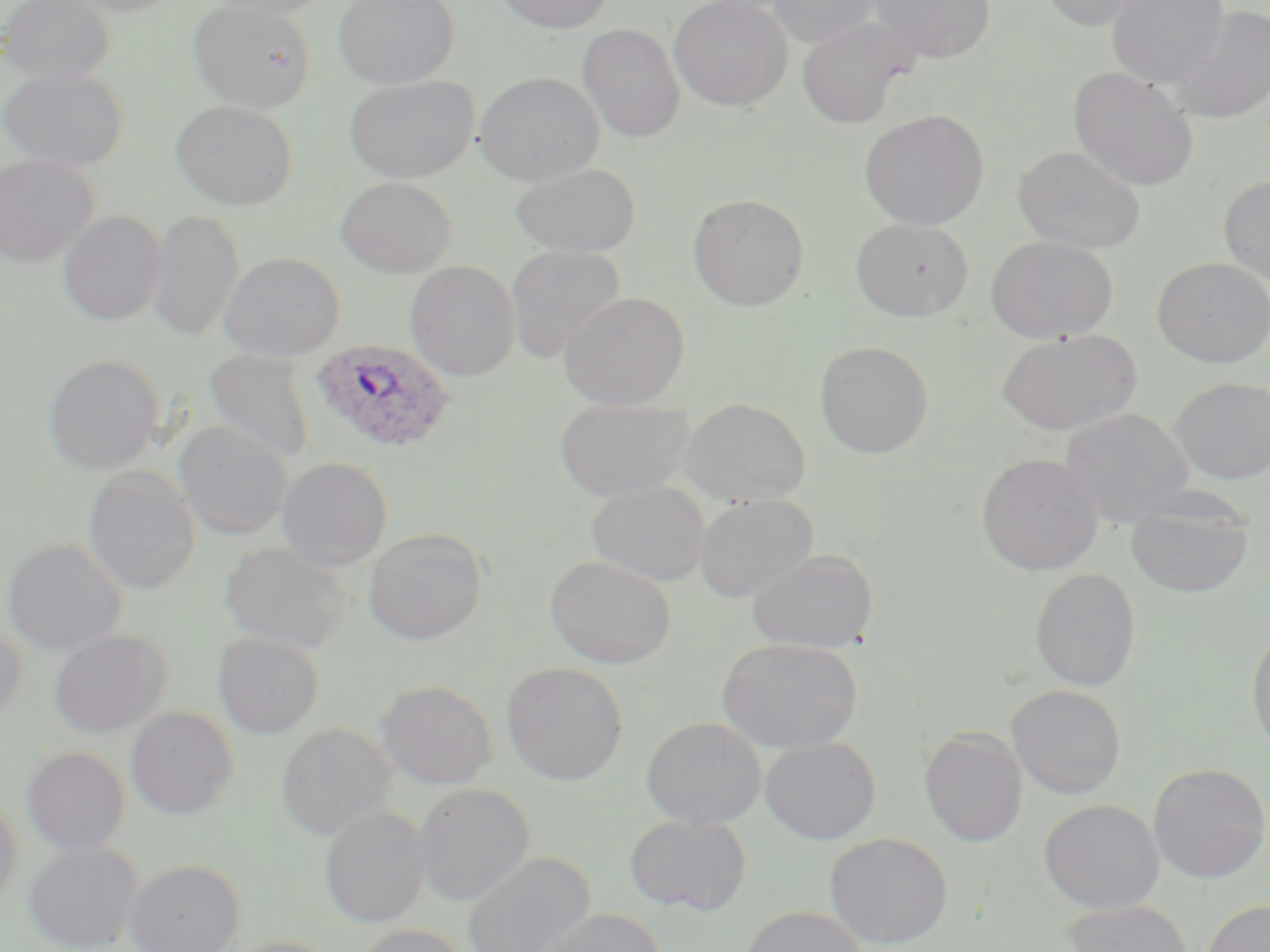
Summary:
  - Coordinate format: approximate bounding boxes as named x1/y1/x2/y2 corners in pixels
  - Plasmodium ovale-infected red blood cell locations: (x1=310, y1=340, x2=455, y2=455)
  - Uninfected red blood cell locations: (x1=1, y1=0, x2=115, y2=85), (x1=61, y1=0, x2=185, y2=17), (x1=188, y1=0, x2=315, y2=113), (x1=209, y1=0, x2=334, y2=20), (x1=333, y1=0, x2=459, y2=89), (x1=492, y1=0, x2=616, y2=34), (x1=669, y1=0, x2=794, y2=111), (x1=767, y1=0, x2=881, y2=48), (x1=868, y1=0, x2=995, y2=63), (x1=1036, y1=0, x2=1149, y2=31), (x1=1107, y1=0, x2=1229, y2=88), (x1=1168, y1=3, x2=1270, y2=125), (x1=796, y1=16, x2=911, y2=129), (x1=577, y1=24, x2=685, y2=143), (x1=1, y1=66, x2=128, y2=173), (x1=1068, y1=67, x2=1199, y2=191), (x1=474, y1=72, x2=604, y2=185), (x1=344, y1=75, x2=479, y2=183), (x1=170, y1=101, x2=297, y2=210), (x1=859, y1=109, x2=990, y2=231), (x1=1013, y1=146, x2=1146, y2=254), (x1=0, y1=155, x2=98, y2=266), (x1=510, y1=162, x2=642, y2=258), (x1=1219, y1=175, x2=1270, y2=286), (x1=335, y1=177, x2=456, y2=277), (x1=688, y1=193, x2=809, y2=311), (x1=147, y1=209, x2=244, y2=343), (x1=58, y1=211, x2=166, y2=326), (x1=851, y1=218, x2=973, y2=321), (x1=986, y1=236, x2=1118, y2=343), (x1=505, y1=245, x2=626, y2=364), (x1=219, y1=252, x2=345, y2=360), (x1=1152, y1=257, x2=1270, y2=367), (x1=405, y1=261, x2=520, y2=381), (x1=559, y1=290, x2=690, y2=410), (x1=997, y1=329, x2=1141, y2=436), (x1=814, y1=341, x2=934, y2=459), (x1=203, y1=350, x2=315, y2=464), (x1=43, y1=355, x2=164, y2=475), (x1=1169, y1=376, x2=1269, y2=484), (x1=554, y1=396, x2=696, y2=501), (x1=680, y1=397, x2=810, y2=506), (x1=1060, y1=407, x2=1195, y2=527), (x1=175, y1=421, x2=293, y2=541), (x1=976, y1=453, x2=1104, y2=574), (x1=276, y1=456, x2=393, y2=570), (x1=82, y1=465, x2=201, y2=595), (x1=586, y1=481, x2=712, y2=586), (x1=1126, y1=490, x2=1255, y2=598), (x1=692, y1=494, x2=819, y2=603), (x1=363, y1=528, x2=488, y2=645), (x1=2, y1=538, x2=127, y2=657), (x1=220, y1=541, x2=354, y2=654), (x1=747, y1=547, x2=878, y2=653), (x1=545, y1=556, x2=676, y2=669), (x1=1031, y1=569, x2=1141, y2=691), (x1=0, y1=621, x2=27, y2=728), (x1=1246, y1=624, x2=1270, y2=759), (x1=48, y1=629, x2=171, y2=737), (x1=213, y1=633, x2=325, y2=738), (x1=716, y1=637, x2=862, y2=754), (x1=501, y1=662, x2=628, y2=785), (x1=378, y1=679, x2=497, y2=789), (x1=1007, y1=684, x2=1126, y2=799), (x1=126, y1=707, x2=238, y2=819), (x1=641, y1=716, x2=766, y2=829), (x1=276, y1=722, x2=397, y2=842), (x1=919, y1=727, x2=1027, y2=848), (x1=760, y1=736, x2=881, y2=844), (x1=22, y1=746, x2=130, y2=857), (x1=1148, y1=762, x2=1270, y2=883), (x1=414, y1=782, x2=534, y2=907), (x1=0, y1=792, x2=22, y2=909), (x1=1039, y1=799, x2=1164, y2=913), (x1=319, y1=806, x2=428, y2=928), (x1=625, y1=814, x2=751, y2=917), (x1=825, y1=832, x2=953, y2=949), (x1=23, y1=840, x2=143, y2=952), (x1=460, y1=851, x2=596, y2=952), (x1=125, y1=859, x2=245, y2=952), (x1=1201, y1=898, x2=1270, y2=952), (x1=1062, y1=899, x2=1193, y2=952), (x1=741, y1=905, x2=870, y2=952), (x1=534, y1=908, x2=666, y2=952), (x1=351, y1=924, x2=472, y2=951), (x1=223, y1=935, x2=345, y2=952)
  - Slide-level diagnosis: Plasmodium ovale
  - Modality: light microscopy
  - Stain: May-Grünwald-Giemsa
  - Magnification: 1000x
  - Image size: 1270×952 pixels
  - Field of view: single
  - Preparation: thin blood film